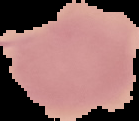
preparation = thin blood film
image size = 139×121 pixels
malaria status = uninfected
image type = cell region segmented out of the field of view; surrounding area masked to black